Report the malaria status of this cell.
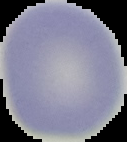
It is uninfected.

Summary:
  - Image type: cell region segmented out of the field of view; surrounding area masked to black
  - Image size: 127×142 pixels
  - Preparation: thin blood smear